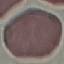 Malaria status: uninfected. Automatically extracted cell patch, resized to 64 × 64 pixels. Giemsa-stained preparation. Photographed with a smartphone camera at the microscope eyepiece. Thin smear of blood.